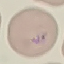

malaria status = parasitized
image type = cell patch, automatically extracted from a larger field of view and resized to 64 × 64 pixels
capture = smartphone through the microscope eyepiece
stain = Giemsa
preparation = thin smear